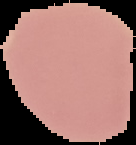

Summary:
  - Preparation: thin blood film
  - Image size: 136×145 pixels
  - Result: negative for malaria parasites
  - Image type: segmented cell region with the area outside set to black